Name the parasite shown.
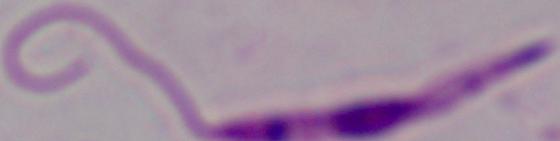

This is Leishmania.

{
  "magnification": "1000x",
  "modality": "micrograph"
}